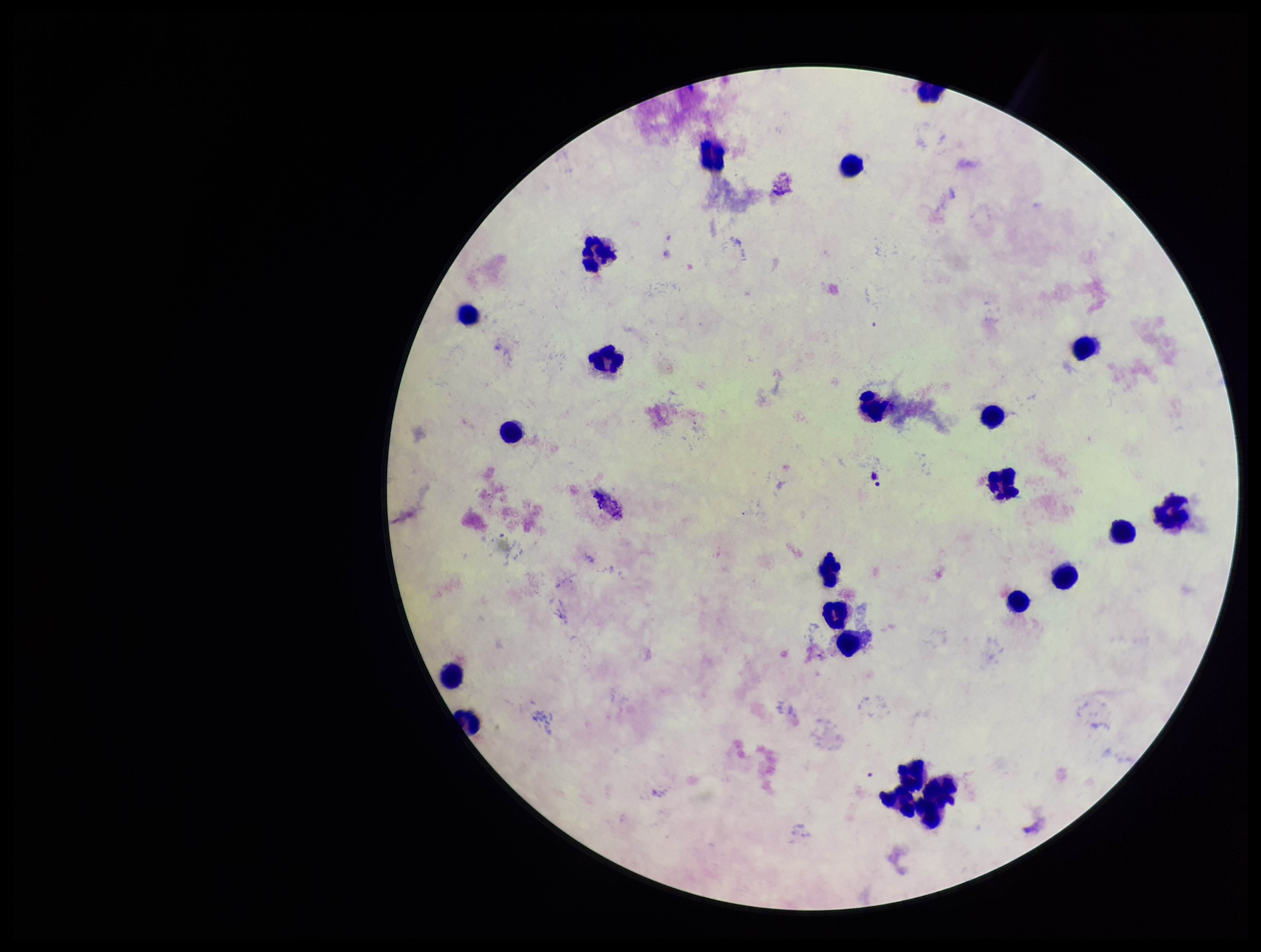

Preparation: thick. One field from this slide. Image is 1261×952 pixels. Smartphone photograph taken through the eyepiece of a microscope. Stained with Giemsa. Plasmodium parasites: none seen. Leukocyte count: 23. Parasite count: 0. Patient malaria status: negative.